Give the position of every malaria parasite.
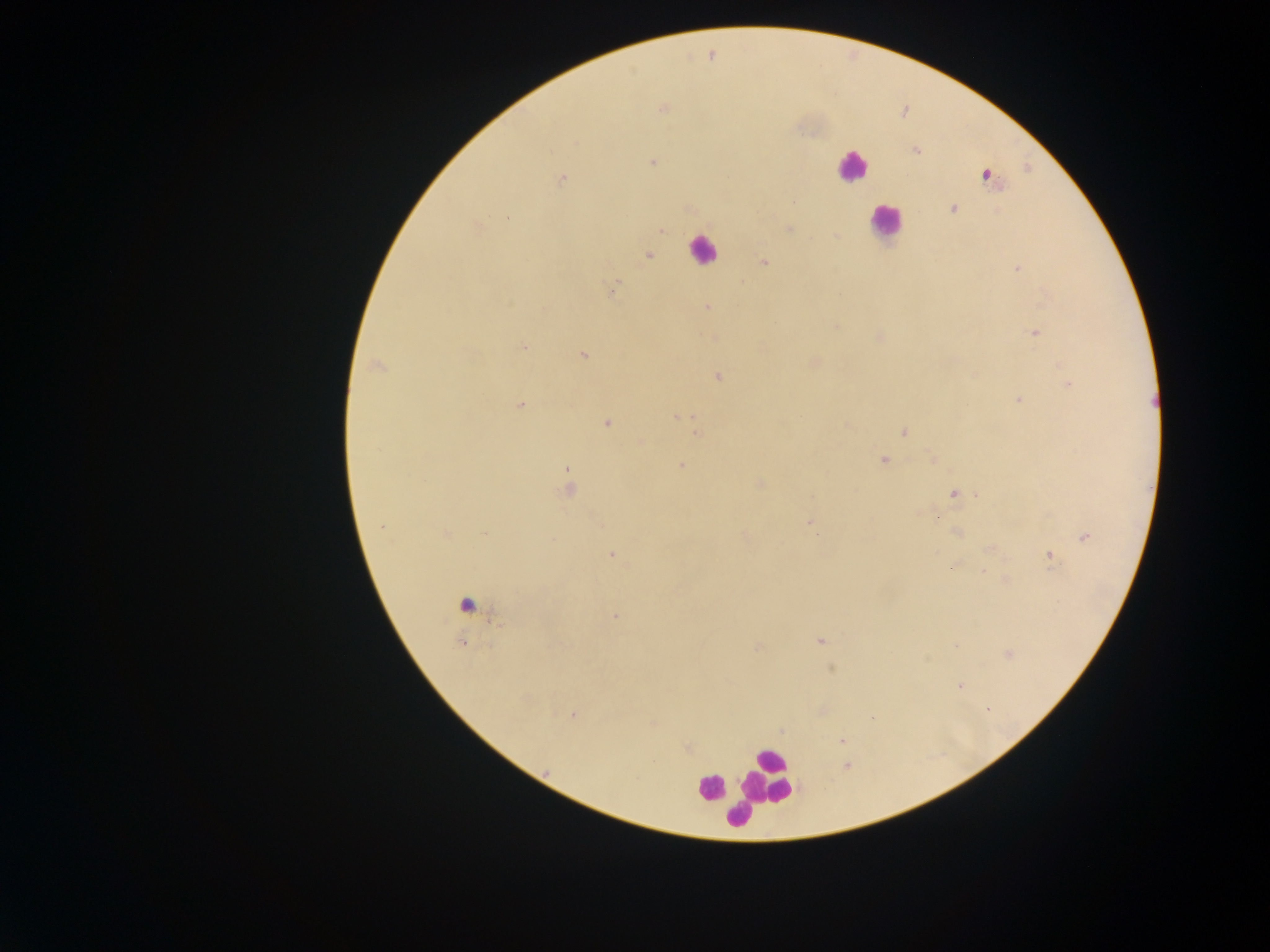
Approximate centers as [x, y] in pixels.
Malaria parasites: [711, 55], [662, 109], [576, 141], [915, 150], [652, 162], [985, 174], [561, 178], [953, 208], [508, 217], [788, 229], [660, 231], [648, 255], [764, 262], [1017, 267], [613, 288], [706, 307], [544, 309], [835, 327], [1035, 332], [878, 336], [523, 346], [582, 354], [813, 361], [377, 366], [718, 375], [974, 375], [1068, 385], [1019, 400], [520, 404], [678, 416], [606, 423], [846, 424], [902, 431], [698, 432], [641, 441], [933, 459], [883, 460], [681, 465], [758, 484], [569, 485], [954, 493], [809, 521], [382, 526], [956, 532], [445, 534], [484, 534], [743, 534], [1084, 536], [992, 548], [611, 553], [1050, 555], [951, 565], [983, 570], [1005, 580], [613, 615], [819, 640], [956, 645], [758, 646], [1009, 654], [830, 669], [959, 685], [987, 708], [822, 709], [573, 715], [653, 723], [781, 729], [842, 740], [686, 748], [845, 766].

Summary:
  - Leukocyte locations: [852, 167], [886, 221], [702, 249], [467, 603], [766, 778], [711, 787], [725, 799], [739, 815]
  - Capture: mobile-phone photograph through a microscope
  - Field of view: single
  - Preparation: thick blood smear
  - Country: Ghana
  - Image size: 1270×952 pixels